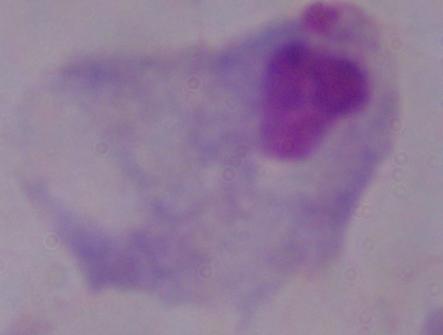 A trichomonad is seen. Micrograph. Captured at 1000x magnification.